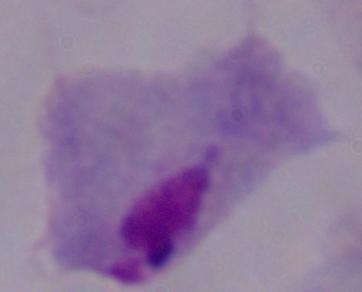 Photomicrograph. Captured at 1000x magnification. A trichomonad is seen.